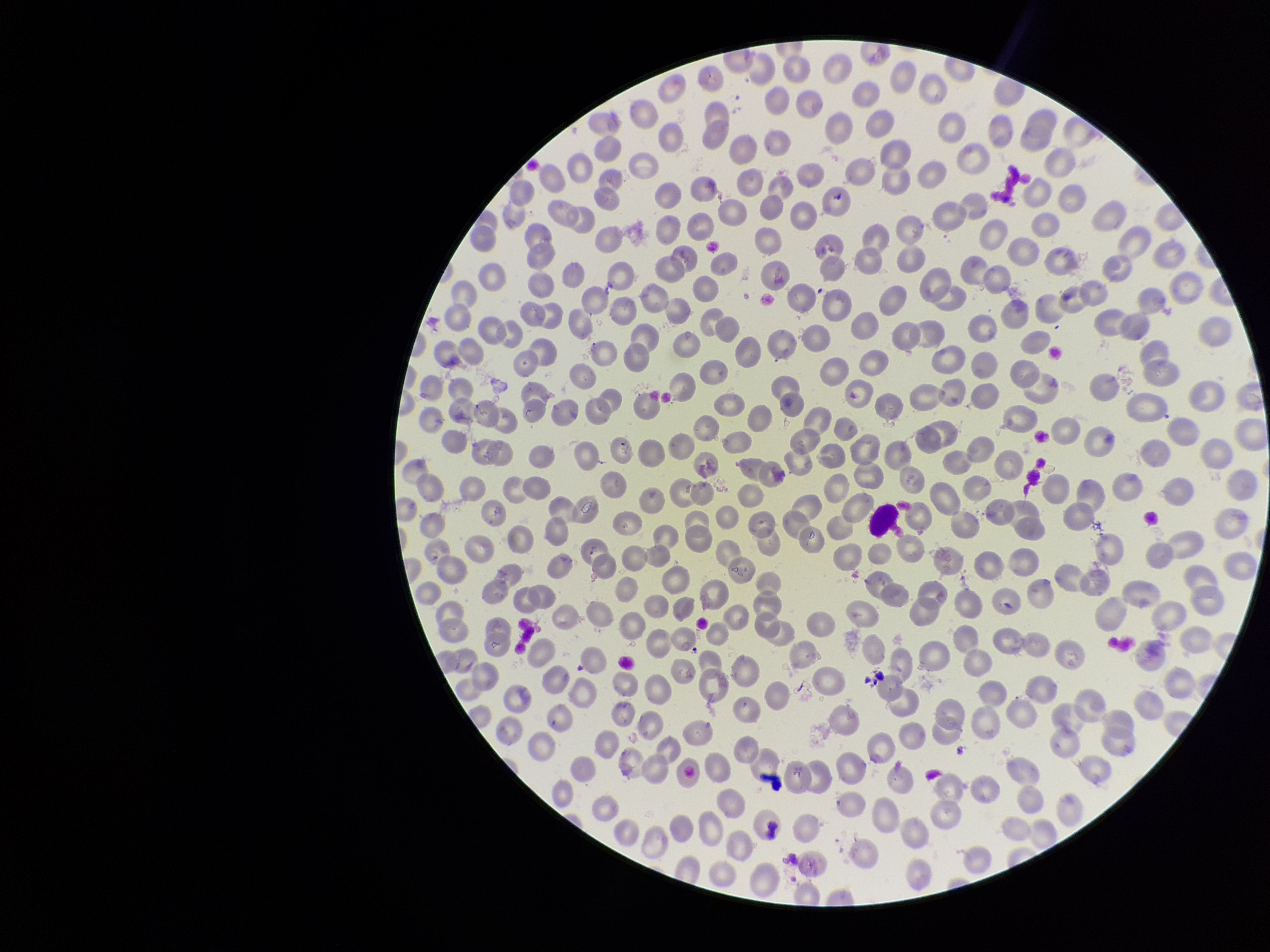
Parasitized red blood cells: none identified. Red blood cell count: 342. Stained with Giemsa. Image is 1270×952 pixels. Smartphone photograph taken through the eyepiece of a microscope. Patient malaria status: negative. Preparation: thin. Parasitized red blood cell count: 0. Single field of view.